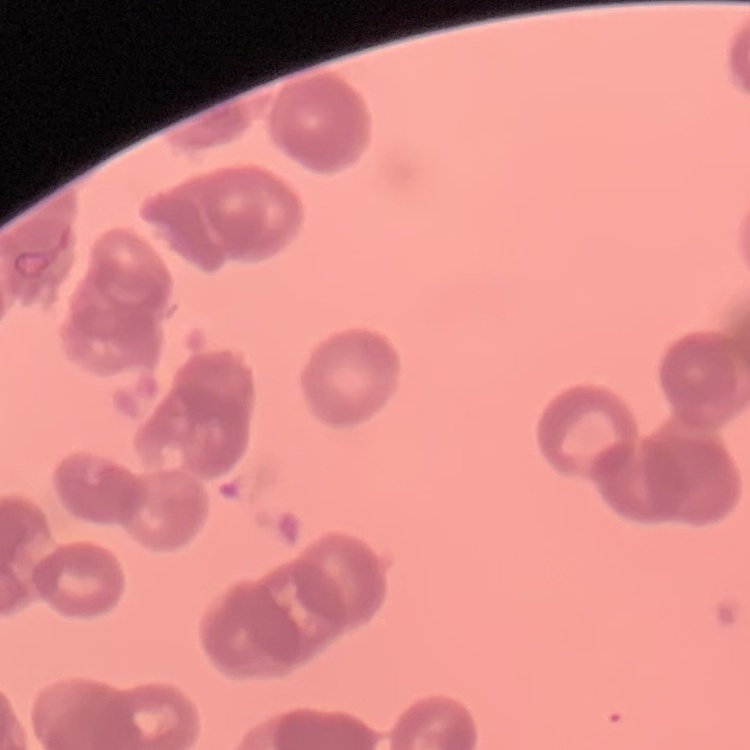
The red blood cells show rouleaux formation. One tile cut from a larger photomicrograph. Thin blood smear. Stained with either Field's or Giemsa.